Classify this cell by malaria status.
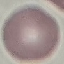
Uninfected.

preparation = thin smear
stain = Giemsa
capture = smartphone camera at the microscope eyepiece
image type = automatically extracted cell patch, resized to 64 × 64 pixels